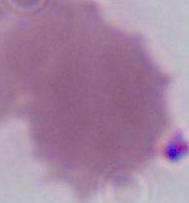

magnification = 1000x
modality = photomicrograph
identification = erythrocyte